Assess this cell for malaria.
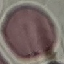
Uninfected.

stain = Giemsa
preparation = thin smear
capture = smartphone through the microscope eyepiece
image type = automatically extracted cell patch, resized to 64 × 64 pixels